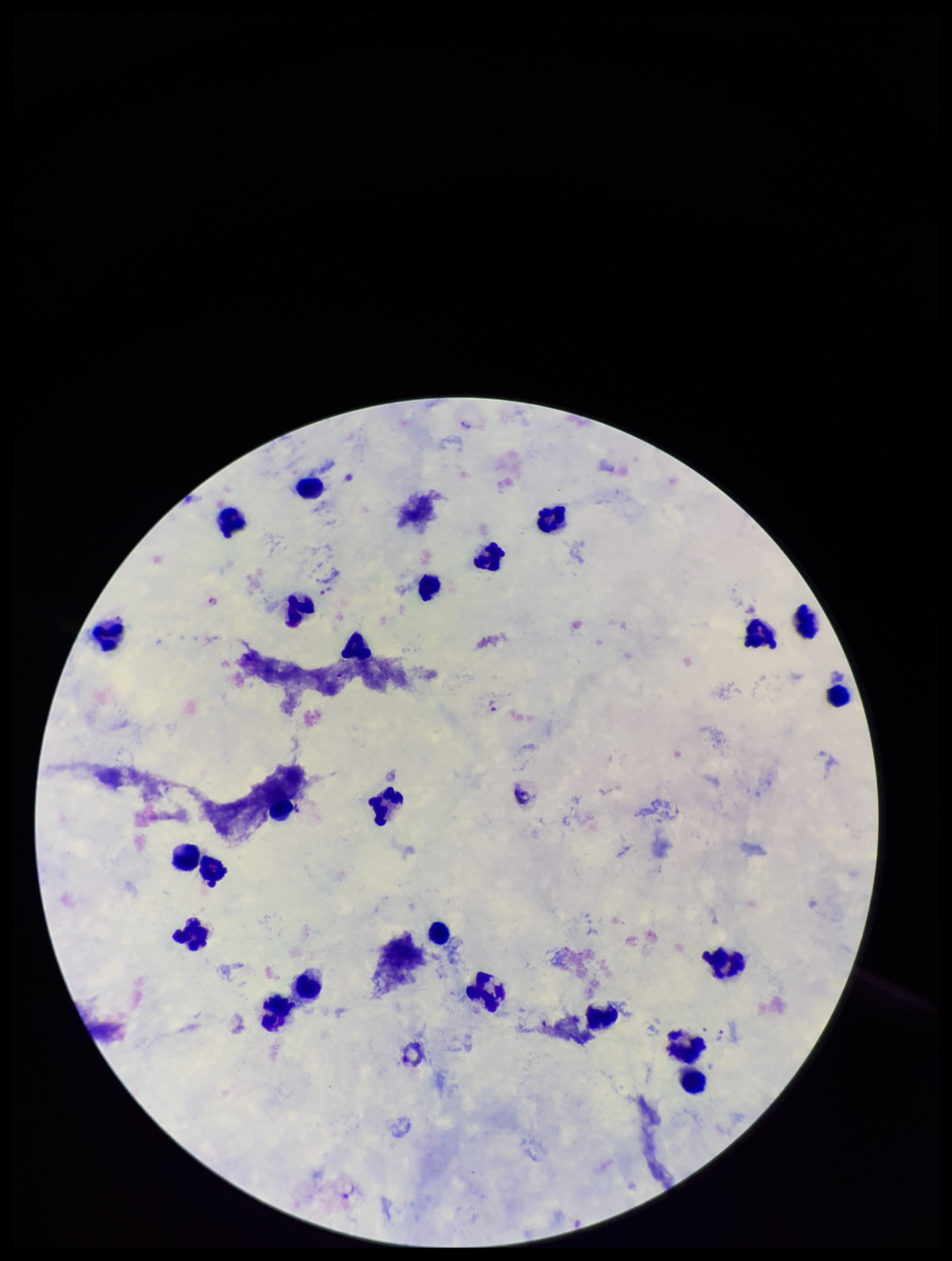

Summary:
  - Plasmodium parasites: detected
  - Patient malaria status: positive
  - Preparation: thick smear
  - Leukocyte count: 25
  - Species reported for this patient: Plasmodium vivax
  - Image size: 952×1261 pixels
  - Field of view: single
  - Stain: Giemsa
  - Capture: smartphone photograph through the microscope eyepiece
  - Parasite count: 3